Comment on the morphology of the erythrocytes.
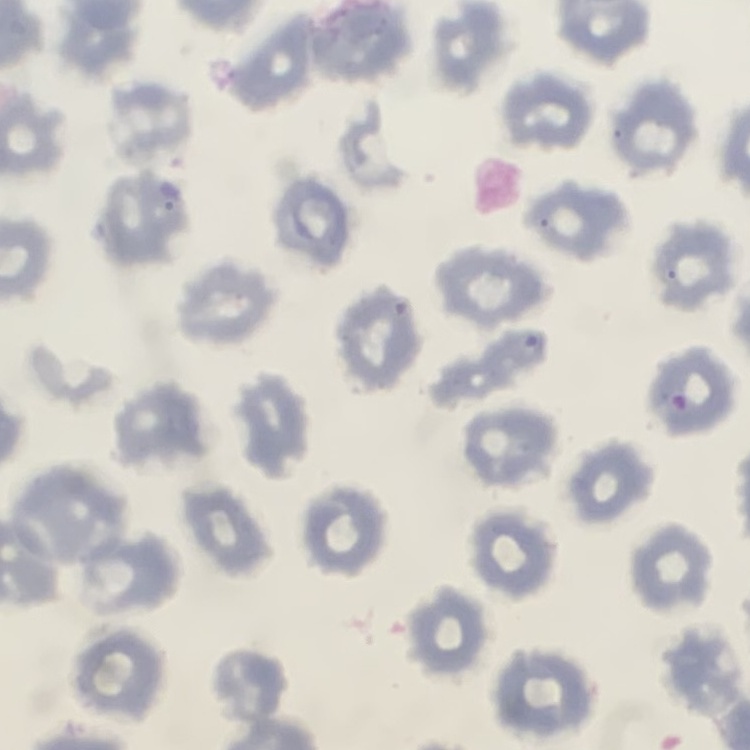
No rouleaux formation.

Summary:
  - Preparation: thin blood film
  - Image type: one tile cut from a larger photomicrograph
  - Stain: Field's or Giemsa